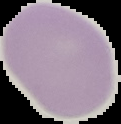
Summary:
  - Image size: 121×124 pixels
  - Malaria status: uninfected
  - Preparation: thin blood film
  - Image type: segmented cell region with the area outside set to black